Comment on the morphology of the erythrocytes.
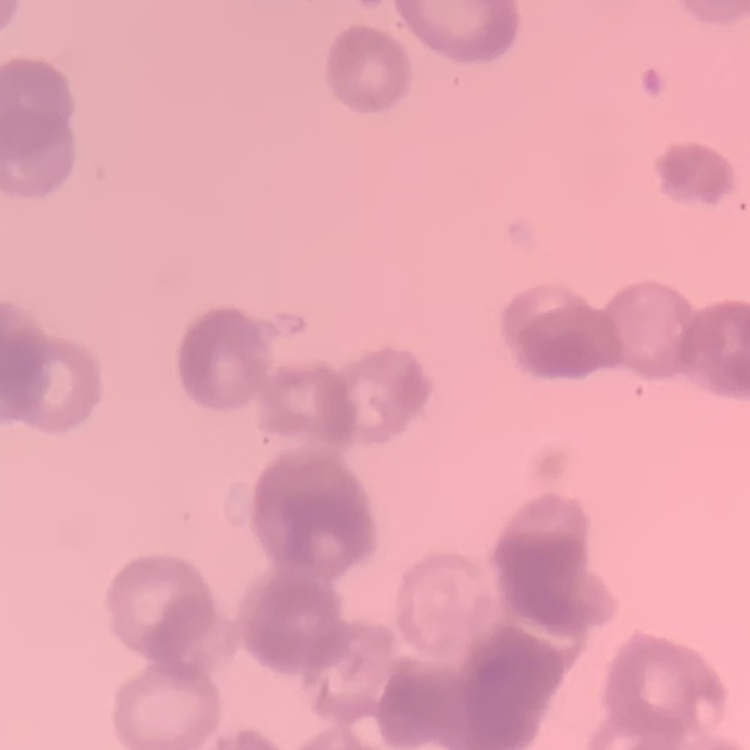

They show rouleaux formation.

preparation = thin peripheral smear
image type = square crop of a larger photomicrograph
stain = Field's or Giemsa